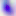
Toxoplasma gondii is shown. Photomicrograph. Captured at 400x magnification.